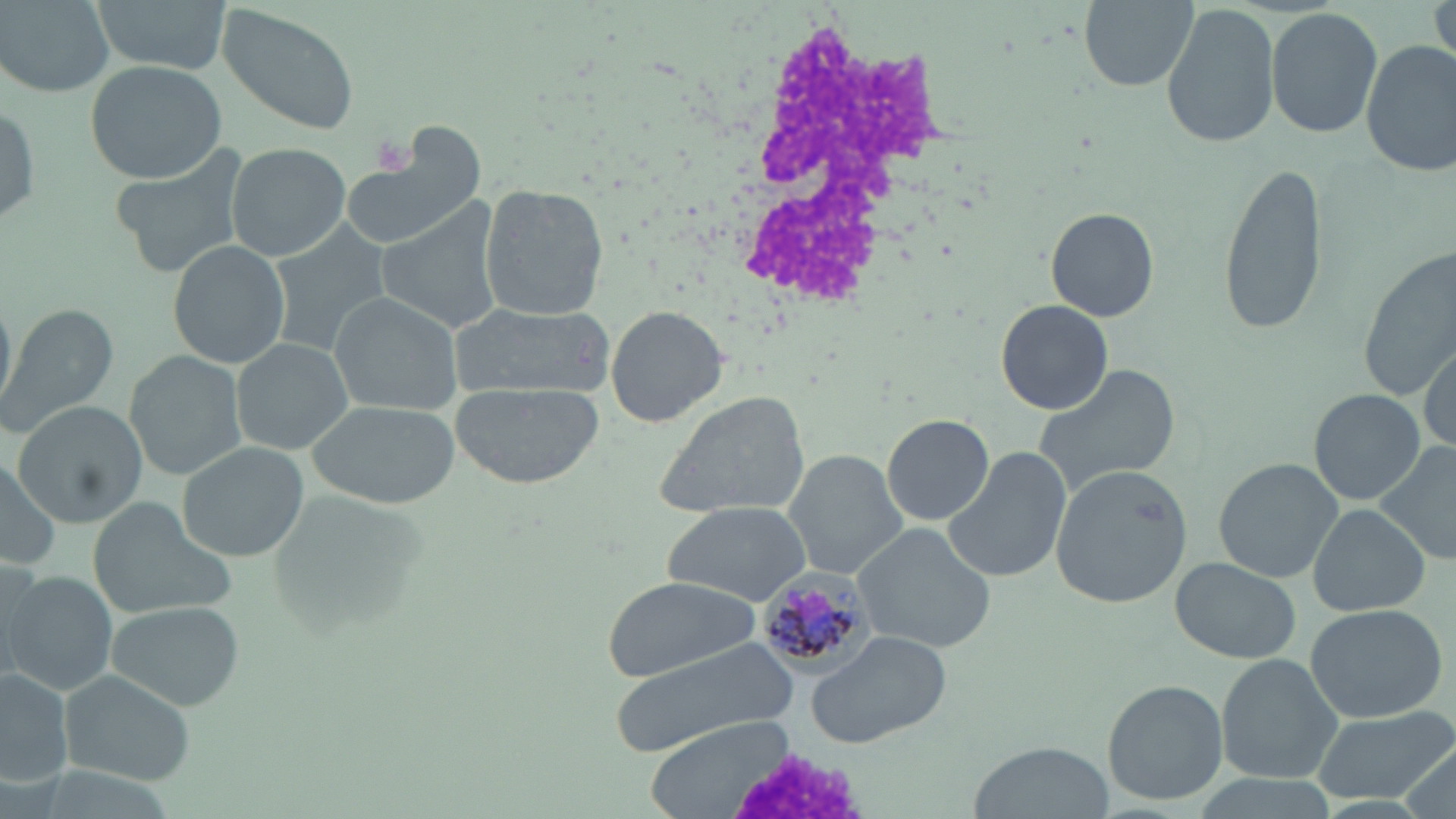
Approximate bounding boxes as named x1/y1/x2/y2 corners in pixels. Plasmodium malariae-infected red blood cell locations: (x1=758, y1=570, x2=872, y2=675). White blood cell locations: (x1=719, y1=14, x2=955, y2=318). Platelet locations: (x1=369, y1=136, x2=411, y2=174). Uninfected red blood cell locations: (x1=94, y1=0, x2=228, y2=74), (x1=1076, y1=0, x2=1200, y2=91), (x1=1430, y1=0, x2=1456, y2=73), (x1=2, y1=1, x2=112, y2=96), (x1=1163, y1=1, x2=1280, y2=149), (x1=217, y1=5, x2=360, y2=137), (x1=1266, y1=7, x2=1381, y2=139), (x1=1362, y1=40, x2=1456, y2=177), (x1=85, y1=59, x2=228, y2=185), (x1=0, y1=102, x2=39, y2=229), (x1=341, y1=129, x2=487, y2=253), (x1=225, y1=142, x2=353, y2=262), (x1=109, y1=147, x2=252, y2=277), (x1=1221, y1=159, x2=1328, y2=338), (x1=479, y1=182, x2=609, y2=322), (x1=376, y1=206, x2=509, y2=334), (x1=1046, y1=206, x2=1160, y2=322), (x1=267, y1=227, x2=390, y2=357), (x1=169, y1=240, x2=289, y2=368), (x1=1360, y1=243, x2=1456, y2=401), (x1=0, y1=288, x2=18, y2=418), (x1=327, y1=292, x2=460, y2=413), (x1=997, y1=299, x2=1112, y2=415), (x1=448, y1=301, x2=612, y2=398), (x1=1, y1=304, x2=117, y2=438), (x1=606, y1=305, x2=728, y2=426), (x1=230, y1=338, x2=353, y2=456), (x1=1418, y1=339, x2=1455, y2=453), (x1=125, y1=351, x2=247, y2=480), (x1=1031, y1=364, x2=1183, y2=497), (x1=449, y1=383, x2=603, y2=488), (x1=650, y1=390, x2=810, y2=520), (x1=1310, y1=391, x2=1425, y2=503), (x1=13, y1=401, x2=151, y2=529), (x1=309, y1=401, x2=458, y2=509), (x1=882, y1=413, x2=993, y2=526), (x1=177, y1=442, x2=310, y2=564), (x1=1372, y1=442, x2=1456, y2=564), (x1=942, y1=448, x2=1070, y2=584), (x1=783, y1=450, x2=909, y2=579), (x1=0, y1=451, x2=63, y2=570), (x1=1211, y1=456, x2=1347, y2=583), (x1=1051, y1=463, x2=1193, y2=608), (x1=87, y1=498, x2=233, y2=623), (x1=660, y1=500, x2=813, y2=605), (x1=1309, y1=504, x2=1432, y2=617), (x1=851, y1=523, x2=997, y2=653), (x1=1172, y1=558, x2=1300, y2=663), (x1=4, y1=571, x2=117, y2=695), (x1=602, y1=577, x2=766, y2=681), (x1=105, y1=601, x2=243, y2=709), (x1=1302, y1=603, x2=1447, y2=721), (x1=809, y1=628, x2=954, y2=748), (x1=608, y1=639, x2=800, y2=763), (x1=1217, y1=654, x2=1345, y2=784), (x1=0, y1=669, x2=75, y2=787), (x1=59, y1=671, x2=196, y2=785), (x1=1101, y1=678, x2=1229, y2=807), (x1=1309, y1=705, x2=1456, y2=804), (x1=647, y1=719, x2=794, y2=817), (x1=972, y1=740, x2=1109, y2=817). Slide-level diagnosis: Plasmodium malariae. Image is 1456×819 pixels. Captured at 1000x magnification. Thin blood smear. May-Grünwald-Giemsa-stained preparation. One field of a larger specimen. Light microscopy.